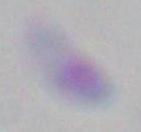

Summary:
  - Identification: Toxoplasma gondii
  - Magnification: 1000x
  - Modality: photomicrograph